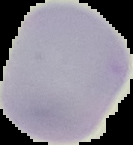
Image is 133×145 pixels. Segmented cell region on a black background. Malaria status: uninfected. From a thin blood film.